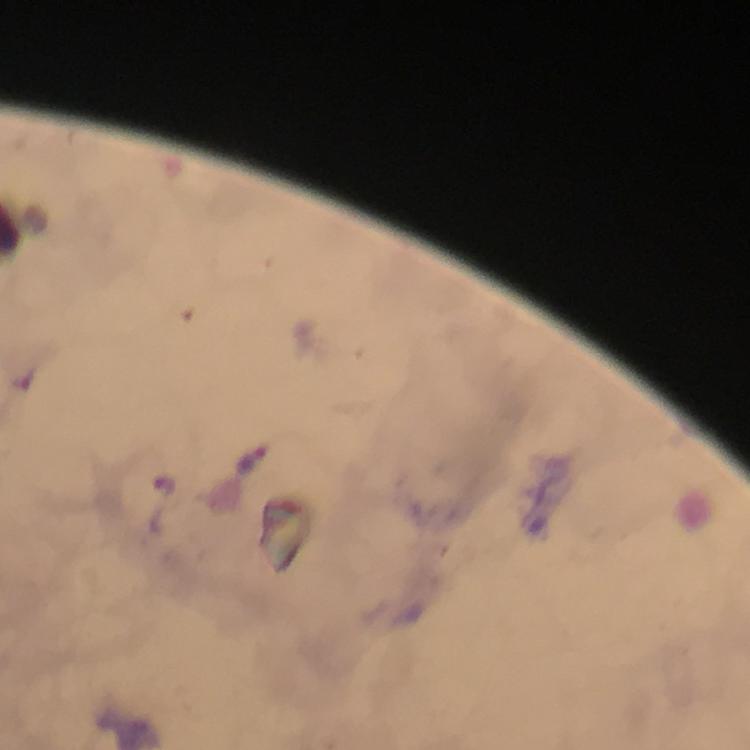
Approximate object centers, in pixels from the top-left corner.
Summary:
  - Plasmodium parasite locations: (x=27, y=377), (x=255, y=461), (x=166, y=482)
  - Immersion oil: used
  - Stain: Giemsa
  - Context: from a diagnostic examination for malaria
  - Preparation: thick blood smear
  - Magnification: 100x
  - Cropped from: one field of view
  - Image size: 750×750 pixels
  - Capture: smartphone photograph through a microscope